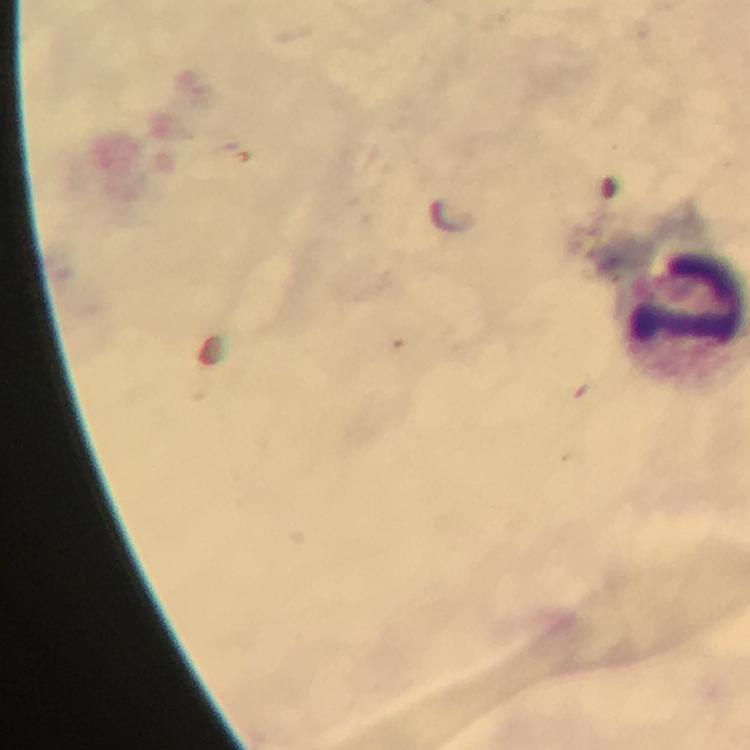
Approximate centers as {x, y} in pixels. Leukocyte locations: {680, 304}. Photographed through the microscope with a smartphone camera. From a malaria diagnostic workup. Image is 750×750 pixels. Malaria parasites: none seen. Thick smear. Giemsa stain. A crop from one field of view. At 100x magnification. Immersion oil applied.